Report the malaria status of this cell.
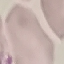
It is uninfected.

{
  "capture": "smartphone camera at the microscope eyepiece",
  "stain": "Giemsa",
  "preparation": "thin blood film",
  "image_type": "automatically extracted cell patch, resized to 64 × 64 pixels"
}